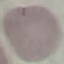

malaria status = uninfected
image type = automatically extracted cell patch, resized to 64 × 64 pixels
preparation = thin smear
stain = Giemsa
capture = smartphone through the microscope eyepiece